Outline each Plasmodium malariae-infected red blood cell.
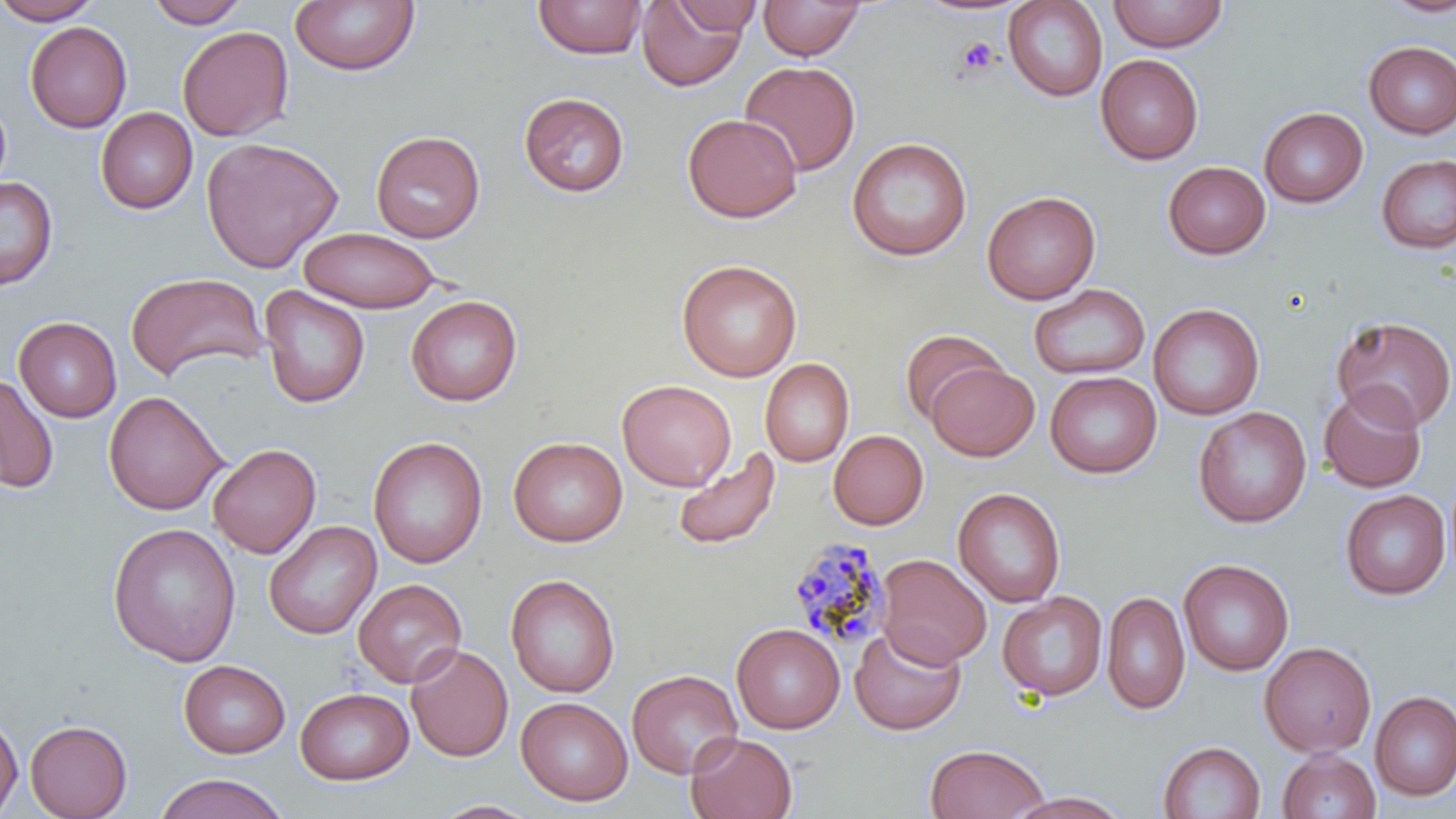

Approximate bounding boxes as (x1, y1, x2, y2) in pixels.
Plasmodium malariae-infected red blood cells: (788, 538, 894, 652).

slide-level diagnosis = Plasmodium malariae
modality = light microscopy
platelet locations = approximate bounding boxes as (x1, y1, x2, y2) in pixels: (957, 37, 1000, 75)
field of view = single
magnification = 1000x
stain = May-Grünwald-Giemsa
preparation = thin blood film
uninfected red blood cell locations = approximate bounding boxes as (x1, y1, x2, y2) in pixels: (0, 0, 104, 25), (145, 0, 249, 28), (289, 0, 420, 76), (533, 0, 649, 60), (759, 0, 864, 60), (1003, 0, 1107, 101), (1107, 0, 1229, 52), (1380, 0, 1456, 19), (637, 1, 749, 91), (669, 1, 763, 35), (25, 21, 132, 133), (177, 25, 294, 141), (1362, 41, 1456, 138), (1095, 54, 1203, 165), (740, 60, 862, 176), (0, 91, 12, 201), (518, 92, 630, 197), (1258, 107, 1367, 207), (95, 108, 198, 214), (682, 114, 803, 223), (371, 130, 485, 243), (201, 136, 343, 273), (847, 136, 972, 261), (1375, 154, 1456, 254), (1163, 161, 1271, 260), (0, 176, 58, 291), (982, 190, 1101, 305), (299, 227, 440, 312), (676, 259, 802, 382), (125, 271, 268, 382), (1029, 283, 1150, 380), (259, 286, 371, 409), (406, 295, 522, 407), (1148, 303, 1264, 420), (1331, 315, 1456, 432), (14, 316, 122, 422), (899, 329, 1006, 424), (760, 358, 854, 467), (926, 362, 1039, 462), (1045, 371, 1161, 478), (0, 373, 58, 493), (617, 379, 736, 492), (1318, 384, 1427, 493), (103, 390, 228, 515), (1193, 407, 1312, 528), (828, 429, 929, 530), (368, 436, 488, 569), (508, 436, 628, 547), (208, 443, 321, 558), (672, 447, 782, 552), (952, 487, 1066, 608), (1340, 489, 1450, 599), (264, 520, 381, 640), (107, 522, 242, 666), (876, 554, 992, 668), (1178, 557, 1294, 676), (505, 573, 620, 698), (353, 579, 467, 688), (1102, 590, 1190, 715), (998, 591, 1108, 701), (731, 623, 845, 733), (849, 626, 966, 735), (1259, 641, 1377, 757), (405, 645, 514, 763), (178, 659, 290, 758), (627, 669, 742, 778), (296, 687, 413, 784), (1370, 690, 1456, 800), (516, 697, 633, 806), (0, 714, 23, 816), (24, 719, 132, 819), (685, 732, 798, 818), (1158, 740, 1265, 819), (924, 743, 1050, 819), (1278, 749, 1380, 819), (154, 772, 288, 819), (1006, 791, 1131, 818), (429, 799, 542, 818)
image size = 1456×819 pixels